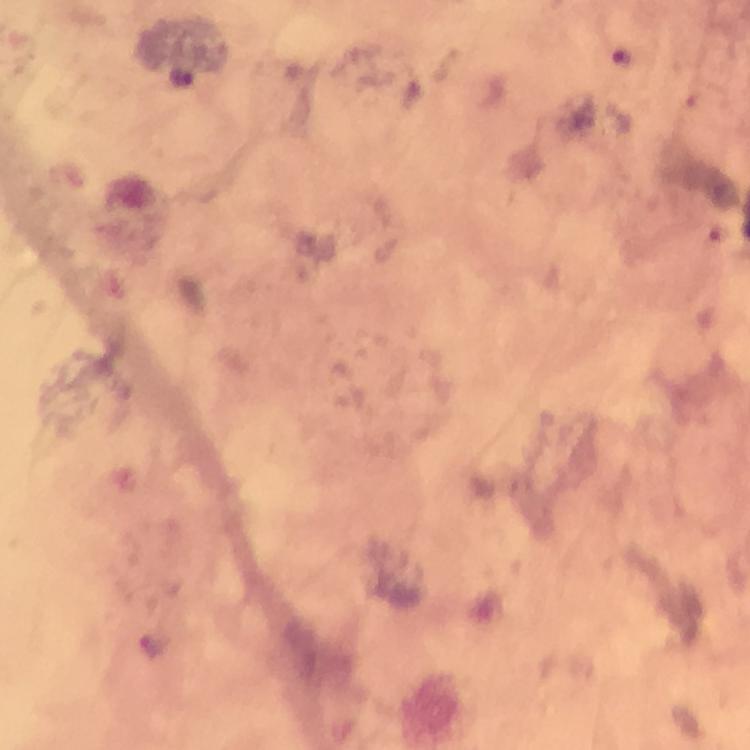

Approximate centers as (x, y) in pixels. Malaria parasite locations: (621, 57). At 100x magnification. Smartphone photograph taken through a microscope. Giemsa stain. Image is 750×750 pixels. A crop from one field of view. Thick blood film. From a malaria diagnostic workup. Immersion oil was used.